Identify the parasite.
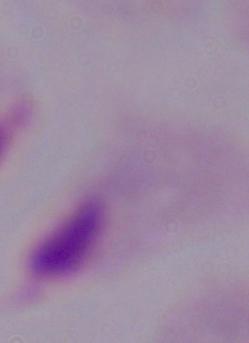

A trichomonad.

magnification = 1000x
modality = photomicrograph